Report the malaria status of this cell.
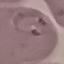
Parasitized.

Acquired by smartphone through the microscope eyepiece. Giemsa stain. Cell patch, automatically extracted from a larger field of view and resized to 64 × 64 pixels. Thin smear of blood.